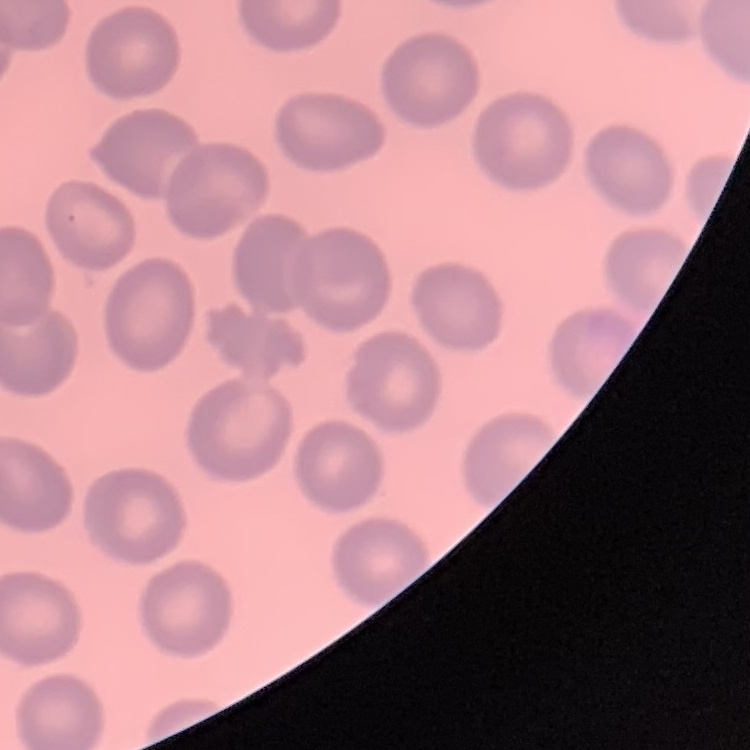

erythrocyte morphology = no rouleaux formation
stain = Field's or Giemsa
preparation = thin peripheral smear
image type = square crop of a larger photomicrograph